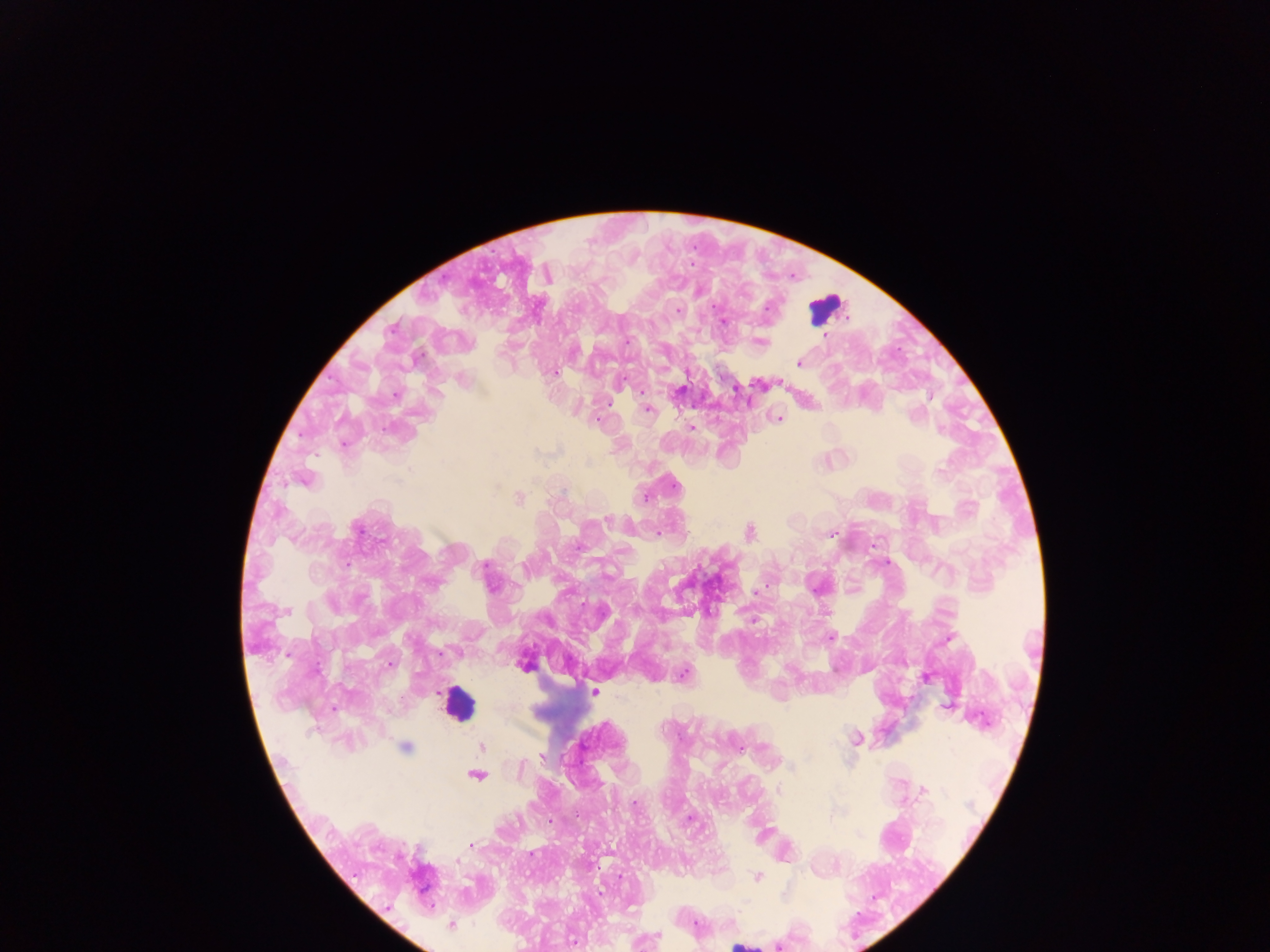
Approximate centers as {x, y} in pixels. Leukocyte locations: {825, 309}, {458, 705}, {740, 945}. Malaria parasite locations: {547, 274}, {678, 311}, {723, 321}, {823, 336}, {760, 342}, {798, 362}, {555, 372}, {462, 379}, {779, 382}, {735, 388}, {642, 393}, {396, 394}, {646, 409}, {777, 418}, {692, 427}, {303, 478}, {519, 499}, {606, 519}, {749, 533}, {831, 533}, {657, 535}, {759, 590}, {753, 621}, {829, 637}, {948, 638}, {524, 663}, {389, 664}, {682, 675}, {923, 677}, {593, 692}, {947, 707}, {856, 739}, {405, 747}, {481, 747}, {739, 748}, {542, 756}, {475, 774}, {923, 791}, {471, 844}, {757, 876}, {451, 924}, {657, 935}. One field of view. Sample from Ghana. Photographed through a microscope with a mobile-phone camera. Image is 1270×952 pixels. Thick blood film.